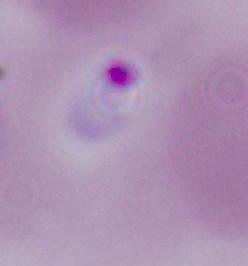

Captured at either 400x or 1000x magnification. A Plasmodium parasite is shown. Photomicrograph.